State which parasite is depicted.
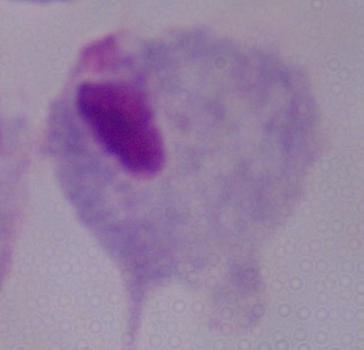
A trichomonad.

Micrograph. Captured at 1000x magnification.